Identify the blood parasite species.
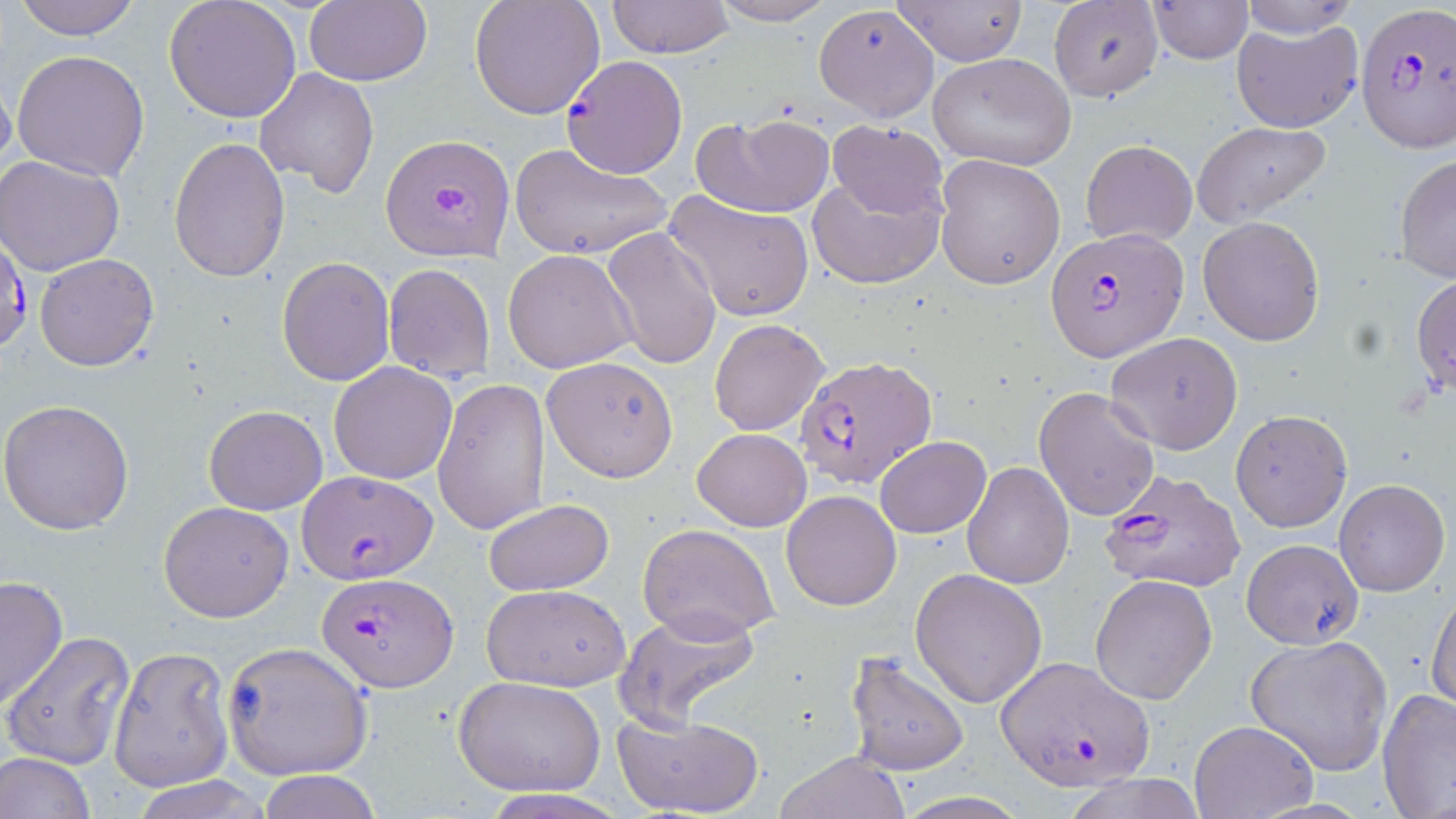

Plasmodium falciparum.

Summary:
  - Coordinate format: approximate bounding boxes as (x1, y1, x2, y2) in pixels
  - Uninfected red blood cell locations: (14, 0, 144, 40), (164, 0, 302, 123), (305, 0, 432, 87), (469, 0, 605, 120), (605, 0, 731, 58), (709, 0, 839, 26), (1147, 0, 1251, 63), (1236, 0, 1361, 38), (895, 1, 1027, 65), (1048, 1, 1163, 102), (813, 5, 940, 122), (1232, 18, 1363, 133), (10, 48, 152, 181), (929, 54, 1077, 171), (255, 67, 381, 197), (0, 73, 16, 185), (692, 112, 835, 217), (828, 120, 948, 220), (1192, 120, 1333, 224), (168, 137, 290, 282), (1081, 139, 1197, 247), (507, 142, 674, 261), (933, 153, 1065, 290), (1394, 153, 1456, 283), (0, 155, 126, 275), (807, 172, 945, 290), (663, 189, 814, 321), (1197, 216, 1325, 345), (602, 227, 722, 372), (503, 249, 639, 372), (34, 254, 159, 372), (276, 256, 394, 386), (383, 262, 496, 381), (1412, 272, 1456, 399), (709, 318, 828, 436), (1104, 332, 1243, 457), (542, 356, 679, 482), (329, 362, 458, 483), (434, 376, 551, 535), (1033, 386, 1162, 522), (0, 401, 134, 536), (203, 406, 328, 513), (1232, 410, 1351, 532), (693, 427, 811, 530), (875, 435, 990, 538), (961, 460, 1072, 588), (1333, 478, 1449, 597), (781, 490, 902, 611), (481, 498, 616, 597), (159, 500, 294, 621), (639, 524, 779, 644), (1242, 538, 1364, 649), (910, 567, 1047, 707), (1090, 574, 1219, 706), (0, 576, 69, 711), (480, 583, 631, 691), (1427, 588, 1456, 711), (614, 606, 766, 731), (3, 630, 135, 770), (1244, 634, 1394, 776), (222, 640, 374, 780), (108, 646, 234, 792), (842, 652, 970, 776), (453, 676, 606, 795), (1378, 689, 1456, 816), (610, 709, 766, 818), (1190, 720, 1317, 819), (774, 750, 910, 819), (0, 751, 97, 819), (254, 769, 380, 819), (129, 776, 273, 818)
  - Plasmodium falciparum-infected red blood cell locations: (1356, 5, 1456, 153), (560, 55, 690, 178), (380, 134, 512, 260), (1046, 227, 1187, 362), (0, 230, 30, 357), (794, 356, 938, 491), (1098, 467, 1243, 593), (296, 469, 437, 582), (317, 573, 457, 692), (995, 654, 1154, 792)
  - Image size: 1456×819 pixels
  - Modality: light microscopy
  - Preparation: thin blood film
  - Stain: May-Grünwald-Giemsa
  - Field of view: one of a larger specimen
  - Magnification: 1000x